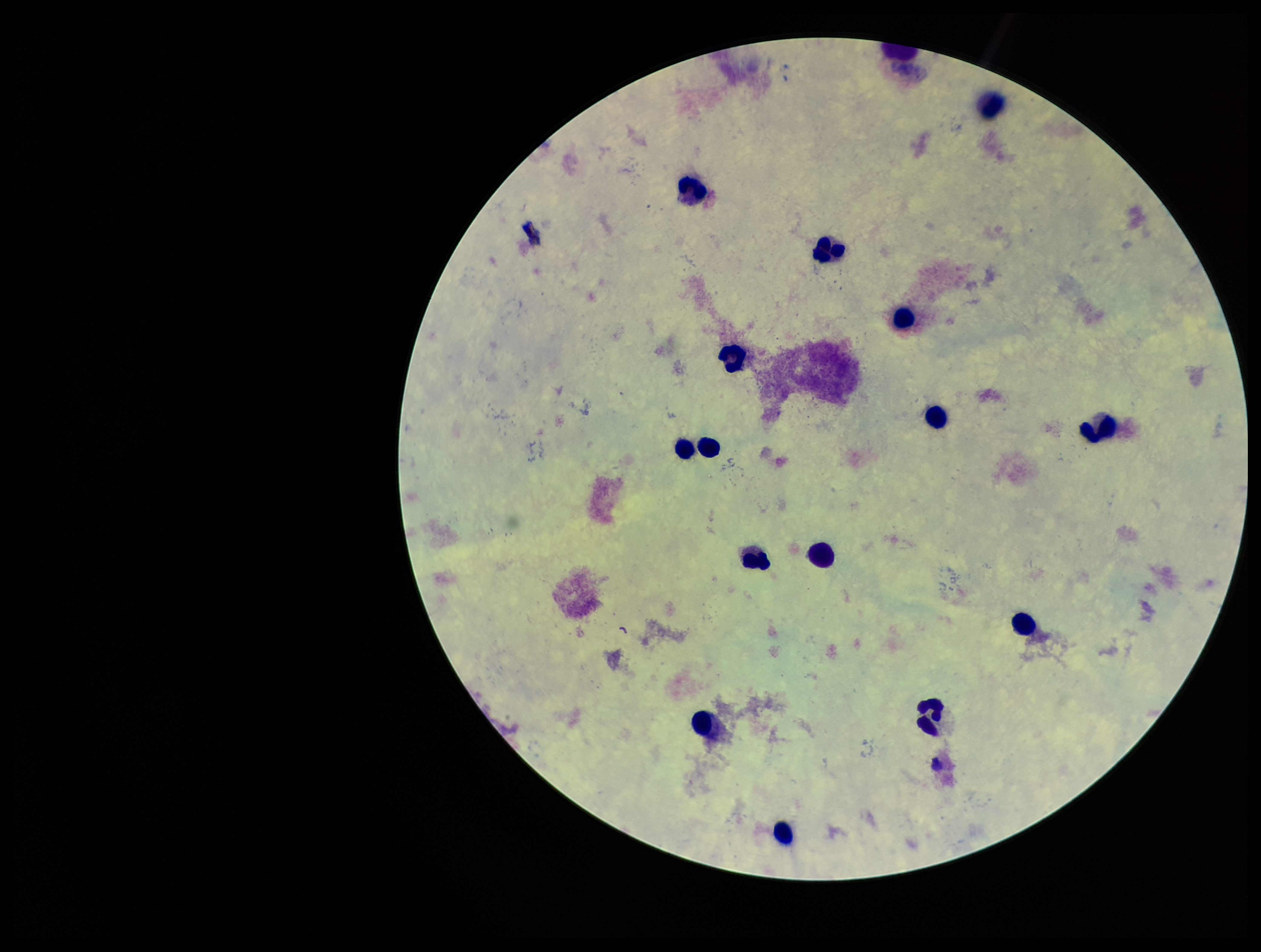

preparation = thick blood smear
capture = smartphone photograph through the microscope eyepiece
stain = Giemsa
leukocyte count = 16
image size = 1261×952 pixels
parasite count = 0
field of view = single
Plasmodium parasites = none identified
patient malaria status = negative